Assess for Plasmodium parasites.
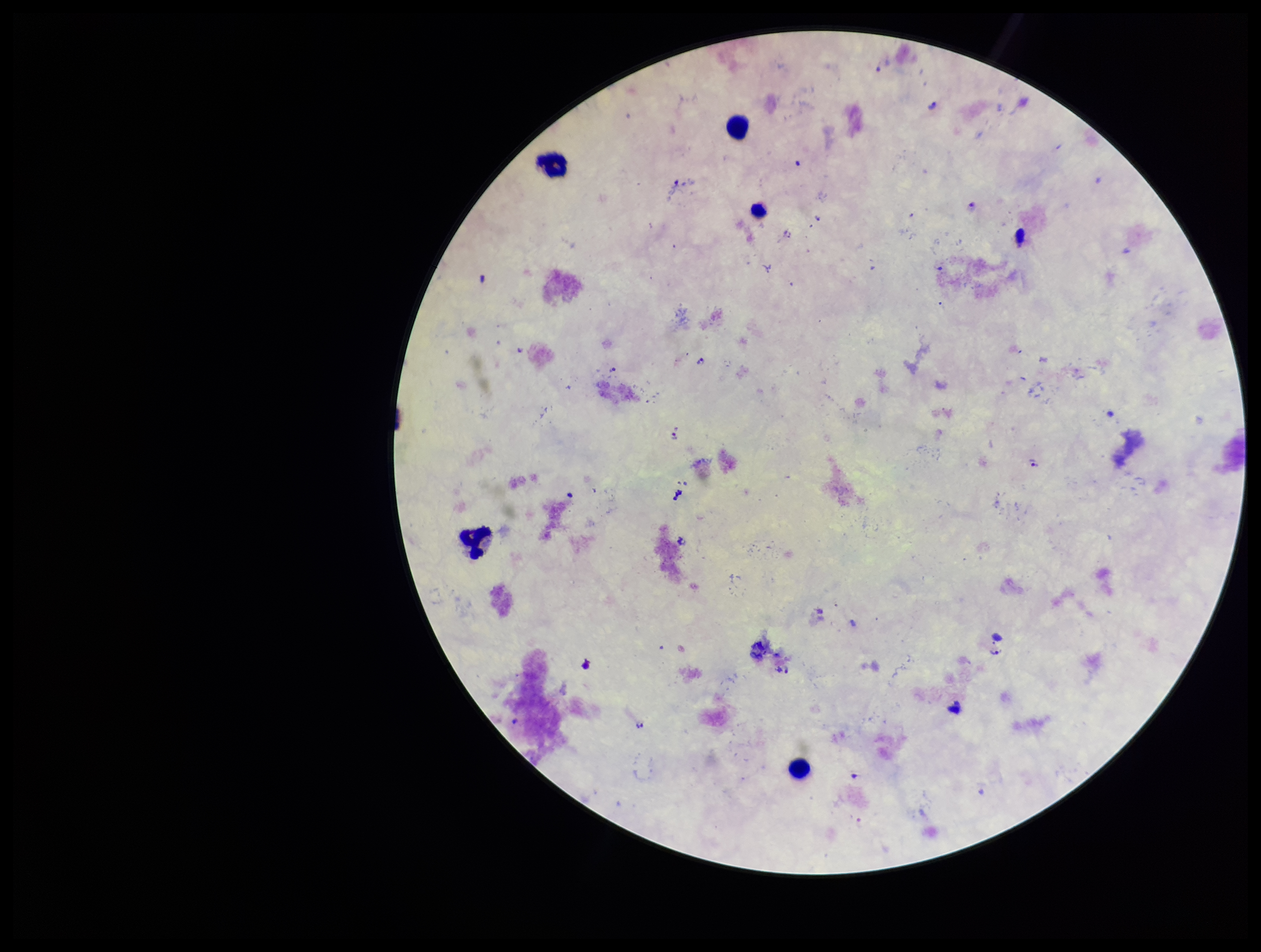
Detected.

Summary:
  - Field of view: one from this slide
  - Capture: smartphone photograph through the microscope eyepiece
  - Leukocyte count: 5
  - Patient malaria status: infected
  - Image size: 1261×952 pixels
  - Stain: Giemsa
  - Species reported for this patient: Plasmodium falciparum
  - Preparation: thick smear
  - Parasite count: 6